Locate and identify every blood parasite.
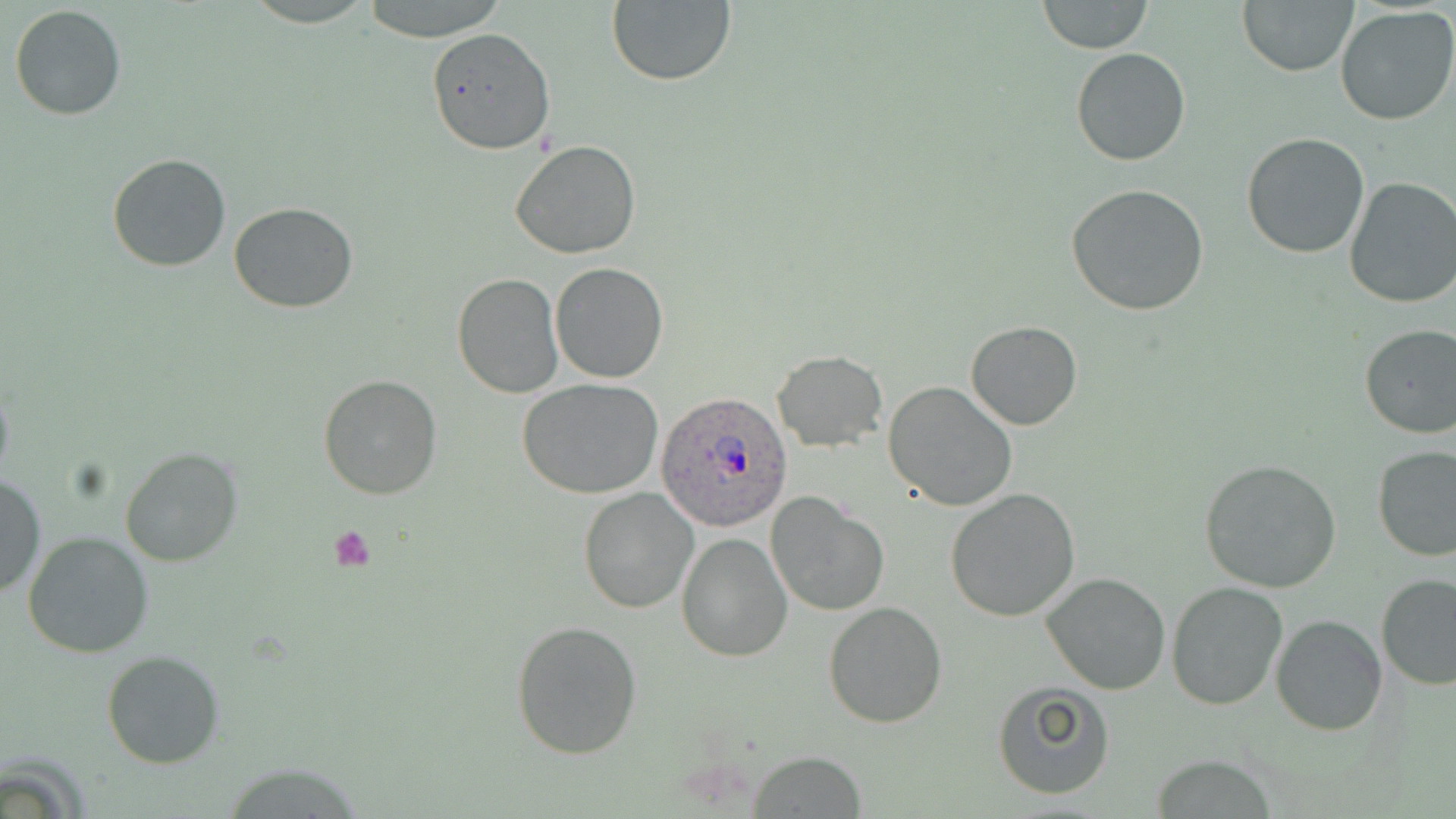
Approximate bounding boxes as named x1/y1/x2/y2 corners in pixels.
Plasmodium ovale-infected red blood cells: (x1=655, y1=392, x2=796, y2=533).
No Plasmodium falciparum, Plasmodium malariae, Plasmodium vivax, Babesia divergens, or Trypanosoma brucei observed.

Platelet locations: (x1=328, y1=526, x2=378, y2=572). Uninfected red blood cell locations: (x1=358, y1=0, x2=512, y2=43), (x1=1238, y1=0, x2=1357, y2=77), (x1=606, y1=1, x2=736, y2=87), (x1=1038, y1=1, x2=1152, y2=54), (x1=10, y1=4, x2=126, y2=120), (x1=1335, y1=7, x2=1456, y2=126), (x1=426, y1=27, x2=554, y2=155), (x1=1071, y1=47, x2=1191, y2=166), (x1=1241, y1=133, x2=1371, y2=259), (x1=509, y1=140, x2=642, y2=260), (x1=107, y1=153, x2=232, y2=273), (x1=1343, y1=176, x2=1456, y2=308), (x1=1066, y1=184, x2=1210, y2=317), (x1=229, y1=202, x2=359, y2=314), (x1=550, y1=263, x2=669, y2=383), (x1=452, y1=272, x2=564, y2=398), (x1=966, y1=321, x2=1081, y2=431), (x1=1357, y1=323, x2=1456, y2=441), (x1=773, y1=350, x2=887, y2=452), (x1=319, y1=374, x2=441, y2=500), (x1=517, y1=378, x2=664, y2=498), (x1=883, y1=380, x2=1017, y2=513), (x1=120, y1=447, x2=243, y2=568), (x1=1373, y1=447, x2=1456, y2=562), (x1=1199, y1=458, x2=1343, y2=594), (x1=0, y1=472, x2=44, y2=600), (x1=578, y1=486, x2=700, y2=614), (x1=943, y1=488, x2=1081, y2=622), (x1=766, y1=492, x2=889, y2=617), (x1=23, y1=530, x2=155, y2=658), (x1=676, y1=533, x2=791, y2=661), (x1=1041, y1=571, x2=1170, y2=696), (x1=1376, y1=574, x2=1455, y2=691), (x1=1167, y1=582, x2=1290, y2=712), (x1=823, y1=601, x2=948, y2=728), (x1=1271, y1=614, x2=1389, y2=735), (x1=509, y1=620, x2=643, y2=760), (x1=101, y1=649, x2=228, y2=769), (x1=991, y1=682, x2=1116, y2=800), (x1=750, y1=751, x2=866, y2=817), (x1=1150, y1=757, x2=1282, y2=816). Slide-level diagnosis: Plasmodium ovale. Image is 1456×819 pixels. Optical microscopy. Thin blood film. Captured at 1000x magnification. Single field of view. May-Grünwald-Giemsa-stained preparation.